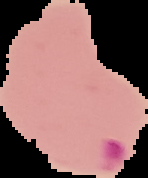
preparation = thin blood film
result = Plasmodium parasites identified
image size = 148×178 pixels
image type = segmented cell region on a black background